Identify the parasite.
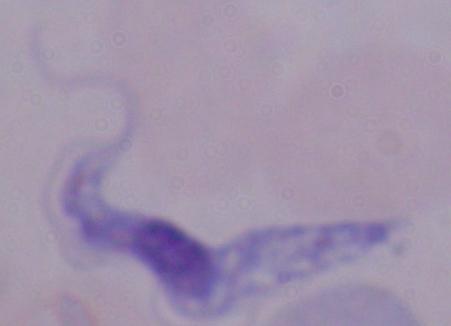
A trypanosome.

modality = photomicrograph
magnification = 1000x